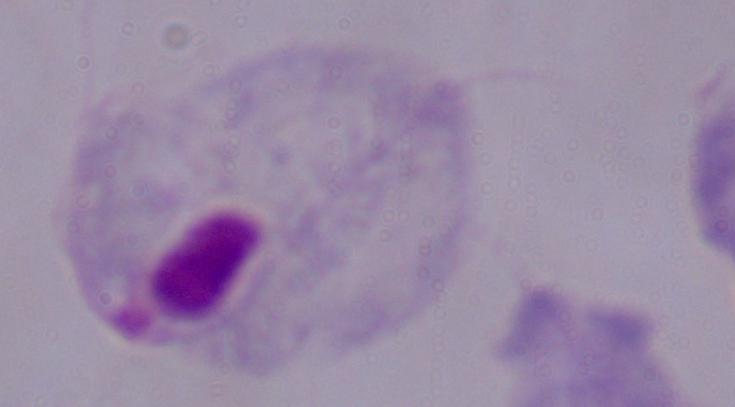
Summary:
  - Modality: photomicrograph
  - Identification: trichomonad
  - Magnification: 1000x